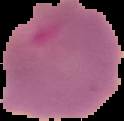
Cell region segmented out of the field of view; the surrounding area is masked to black. From a thin blood smear. Image is 124×121 pixels. Result: Plasmodium parasites identified.